Report the malaria status of this cell.
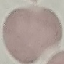
Uninfected.

Thin blood film. Acquired by smartphone through the microscope eyepiece. Cell patch, automatically extracted from a larger field of view and resized to 64 × 64 pixels. Giemsa-stained preparation.